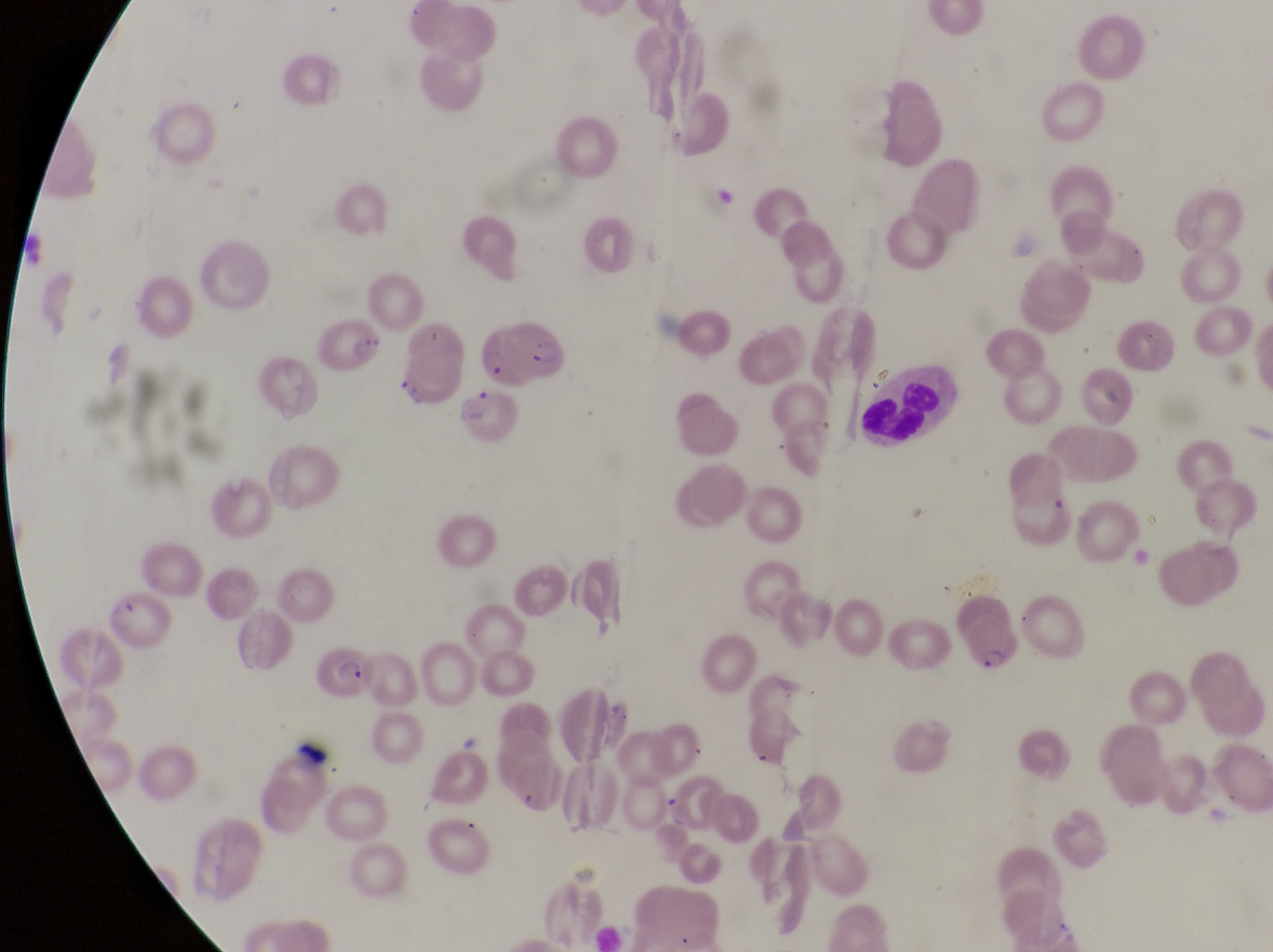 Approximate bounding boxes as (left, top, right, bottom) in pixels. Leukocyte locations: (868, 360, 958, 450). Parasitised red blood cell locations: (320, 310, 387, 372), (479, 320, 574, 394), (956, 597, 1023, 675), (317, 640, 382, 702), (668, 779, 725, 829). One field of view. Captured by a smartphone held over the eyepiece of an Olympus CX-23 microscope. Image is 1273×952 pixels. Thin blood film. Collected in Uganda. At a magnification of 1000x.